Describe the morphology of the red blood cells.
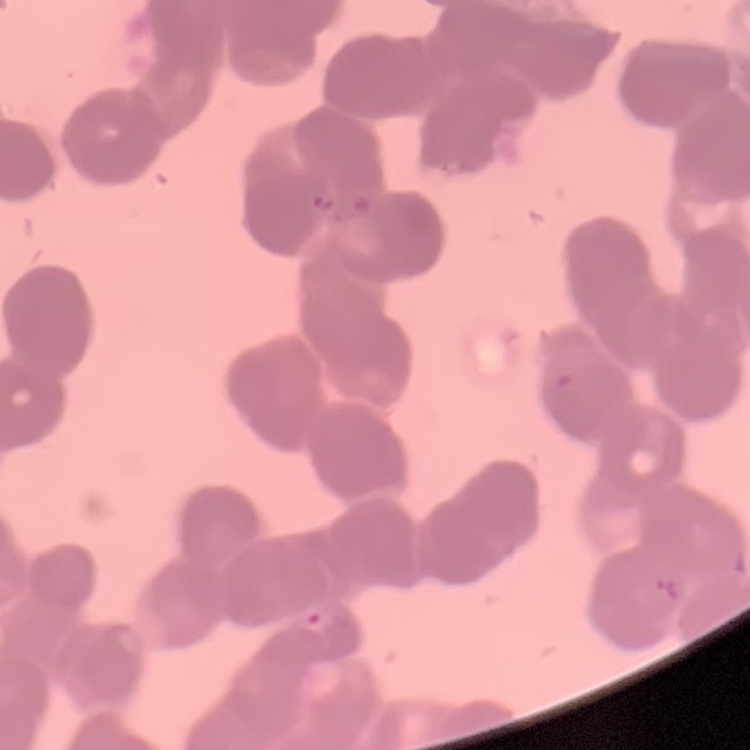

Rouleaux formation.

stain = Field's or Giemsa
preparation = thin blood smear
image type = one tile cut from a larger photomicrograph